Assess this cell for malaria.
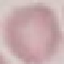

It is uninfected.

Photographed with a smartphone camera at the microscope eyepiece. Giemsa-stained preparation. Thin blood film. Cell patch, automatically extracted from a larger field of view and resized to 64 × 64 pixels.